Outline each Plasmodium malariae-infected red blood cell.
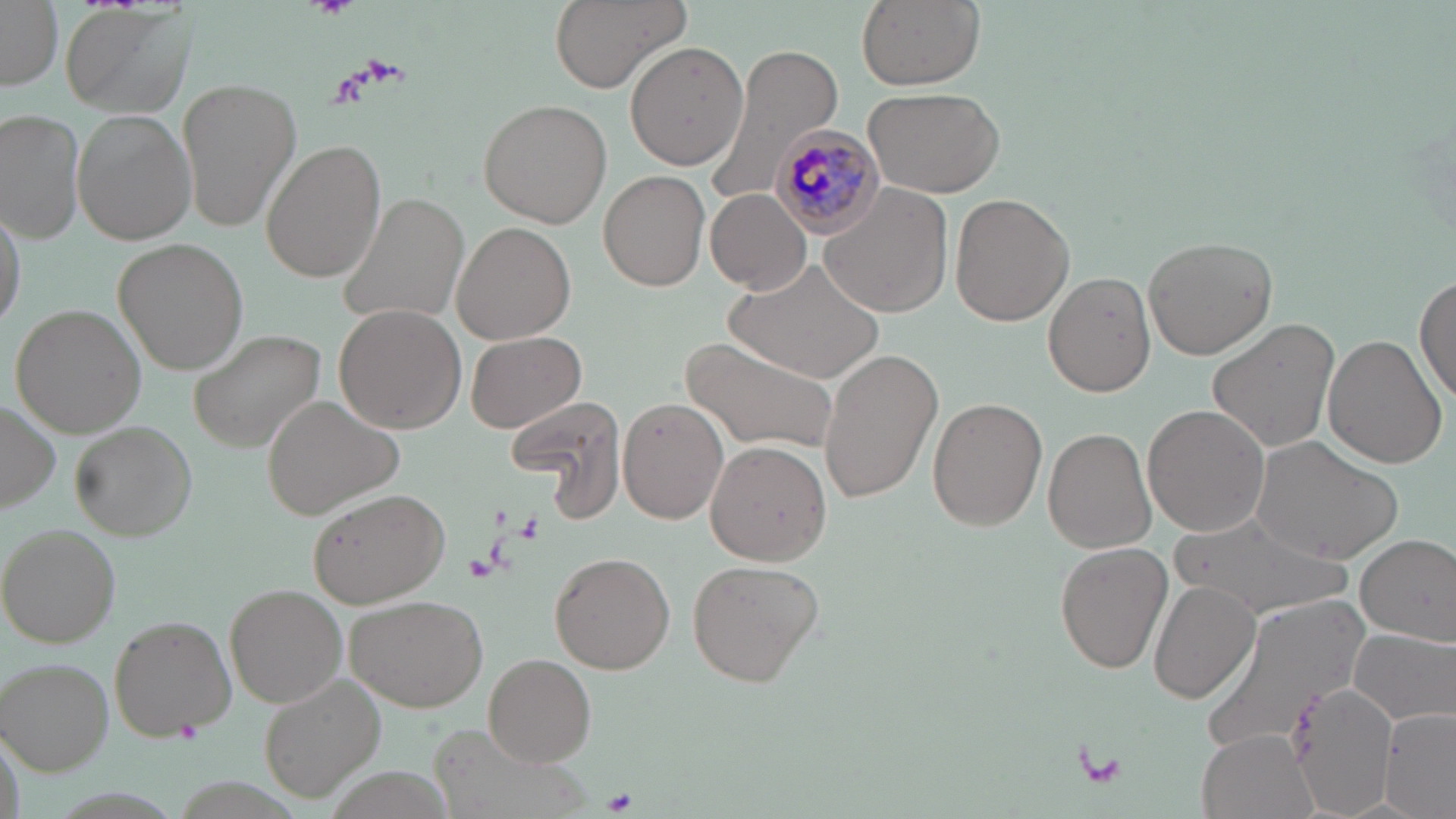
Approximate bounding boxes as [x1, y1, x2, y2] in pixels.
Plasmodium malariae-infected red blood cells: [769, 125, 888, 237].

Summary:
  - Platelet locations: [309, 0, 361, 19], [365, 56, 410, 87], [175, 721, 201, 742], [1078, 744, 1131, 791], [605, 790, 639, 813]
  - Uninfected red blood cell locations: [0, 0, 61, 90], [547, 0, 693, 92], [854, 0, 984, 90], [64, 7, 194, 116], [624, 40, 749, 172], [703, 42, 847, 208], [179, 75, 303, 232], [864, 85, 1005, 198], [477, 99, 613, 228], [2, 109, 88, 243], [72, 111, 194, 245], [261, 137, 387, 284], [596, 172, 712, 290], [820, 182, 953, 317], [704, 188, 811, 295], [339, 193, 469, 329], [948, 193, 1075, 326], [1, 201, 26, 336], [452, 220, 578, 345], [1142, 236, 1278, 360], [114, 238, 249, 374], [734, 255, 884, 385], [1042, 271, 1157, 397], [1415, 275, 1456, 409], [11, 305, 147, 438], [334, 305, 467, 432], [1207, 317, 1341, 454], [185, 326, 327, 451], [465, 330, 586, 433], [1324, 333, 1449, 469], [683, 337, 840, 455], [817, 346, 943, 503], [263, 396, 405, 520], [927, 396, 1049, 532], [504, 397, 626, 506], [620, 397, 729, 524], [2, 400, 61, 516], [1143, 405, 1270, 538], [70, 420, 200, 542], [1043, 428, 1156, 553], [1251, 437, 1401, 562], [705, 441, 834, 565], [309, 489, 450, 608], [1167, 509, 1354, 623], [3, 524, 121, 647], [1355, 533, 1456, 645], [1054, 541, 1173, 674], [550, 551, 675, 674], [688, 558, 823, 685], [1149, 579, 1260, 703], [225, 583, 346, 707], [347, 593, 487, 712], [1202, 596, 1371, 758], [109, 617, 236, 739], [1350, 627, 1455, 726], [484, 653, 598, 766], [0, 657, 112, 775], [260, 675, 386, 804], [1289, 682, 1395, 818], [1377, 702, 1456, 817], [1197, 728, 1317, 819]
  - Slide-level diagnosis: Plasmodium malariae
  - Magnification: 1000x
  - Field of view: one of a larger specimen
  - Image size: 1456×819 pixels
  - Preparation: thin blood smear
  - Stain: May-Grünwald-Giemsa
  - Modality: light microscopy